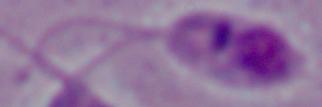
Summary:
  - Modality: photomicrograph
  - Identification: Leishmania
  - Magnification: 1000x